Identify the parasite.
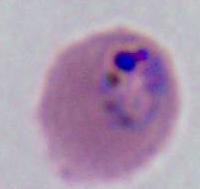

Plasmodium.

modality = micrograph
magnification = 400x or 1000x